Identify the parasite.
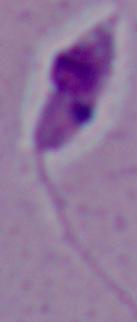
Leishmania.

{
  "magnification": "1000x",
  "modality": "micrograph"
}